Outline each blood parasite and name the species.
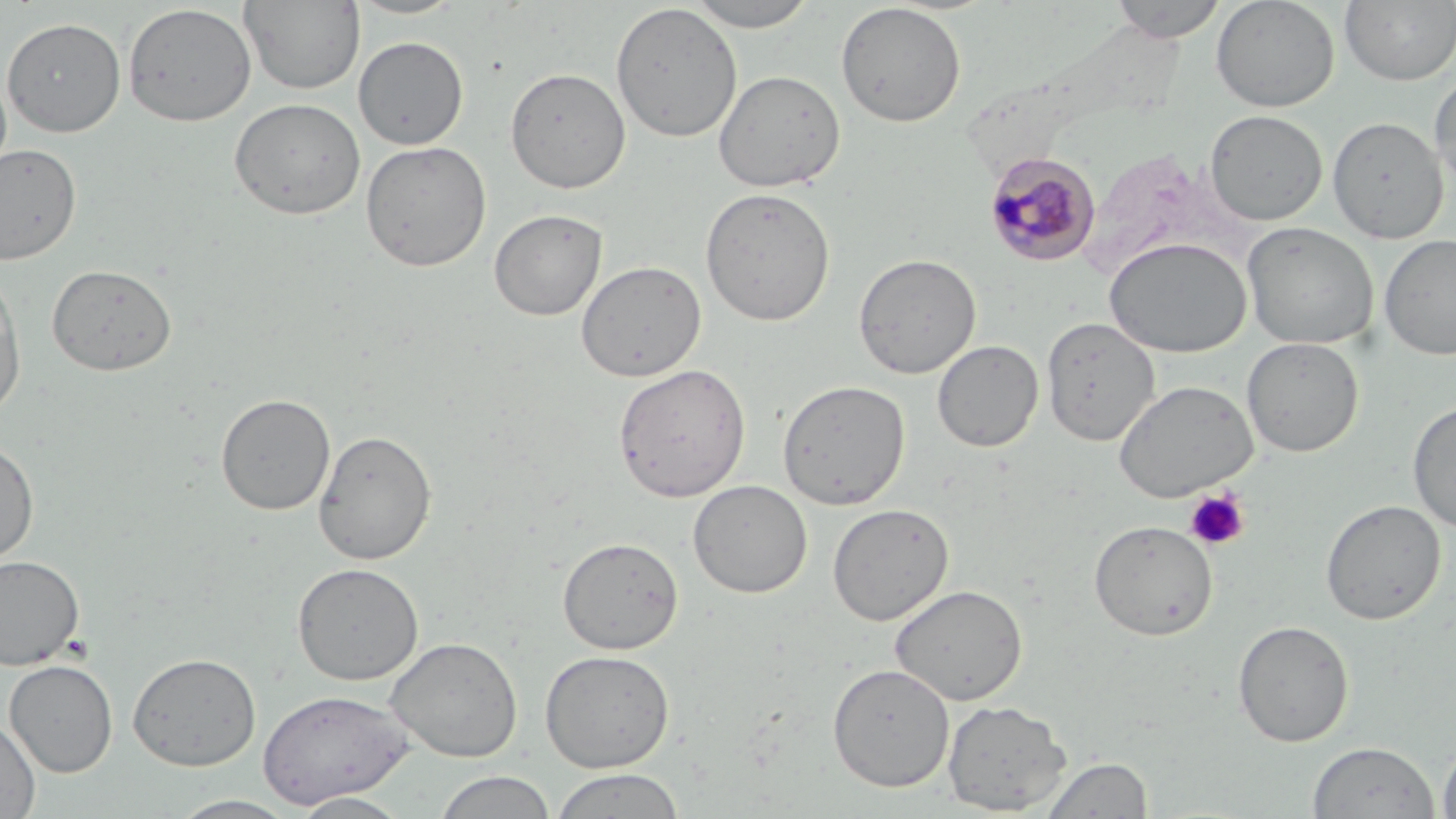
Approximate bounding boxes as [x1, y1, x2, y2] in pixels.
Plasmodium malariae-infected red blood cells: [984, 151, 1101, 267].
No Plasmodium falciparum, Plasmodium ovale, Plasmodium vivax, Babesia divergens, or Trypanosoma brucei observed.

slide-level diagnosis = Plasmodium malariae
field of view = single
uninfected red blood cell locations = approximate bounding boxes as [x1, y1, x2, y2] in pixels: [346, 0, 467, 20], [682, 0, 822, 31], [1108, 0, 1228, 43], [1211, 0, 1340, 113], [1340, 0, 1456, 86], [239, 1, 365, 94], [835, 2, 967, 127], [610, 3, 743, 143], [122, 4, 257, 127], [1, 16, 126, 137], [353, 36, 469, 150], [505, 66, 631, 194], [0, 67, 13, 186], [713, 69, 845, 192], [1429, 73, 1456, 195], [229, 97, 366, 220], [1204, 110, 1329, 226], [1328, 115, 1450, 244], [360, 140, 492, 272], [0, 142, 82, 265], [1078, 147, 1238, 281], [699, 186, 836, 326], [489, 208, 607, 321], [1241, 222, 1379, 350], [1378, 233, 1456, 361], [1104, 236, 1252, 357], [853, 252, 981, 378], [575, 260, 706, 382], [46, 263, 178, 376], [0, 274, 26, 419], [1041, 316, 1161, 446], [1242, 336, 1364, 457], [932, 340, 1043, 452], [613, 363, 751, 503], [777, 379, 910, 510], [1114, 379, 1258, 502], [216, 393, 336, 515], [1407, 399, 1456, 533], [313, 429, 437, 565], [0, 439, 39, 568], [688, 479, 812, 598], [1320, 499, 1446, 625], [828, 504, 954, 626], [1089, 519, 1218, 640], [557, 536, 684, 654], [0, 554, 85, 671], [292, 562, 424, 685], [890, 584, 1028, 706], [1232, 620, 1354, 747], [385, 636, 523, 761], [539, 649, 675, 772], [127, 652, 261, 771], [4, 660, 118, 777], [827, 662, 955, 792], [257, 689, 413, 809], [942, 699, 1073, 815], [0, 716, 40, 818], [1437, 739, 1456, 819], [1307, 741, 1439, 819], [1040, 757, 1152, 818], [550, 768, 686, 818], [433, 771, 557, 819], [291, 792, 412, 818], [166, 794, 302, 818]
stain = May-Grünwald-Giemsa
magnification = 1000x
image size = 1456×819 pixels
modality = light microscopy
preparation = thin blood film
platelet locations = approximate bounding boxes as [x1, y1, x2, y2] in pixels: [1184, 488, 1250, 551]